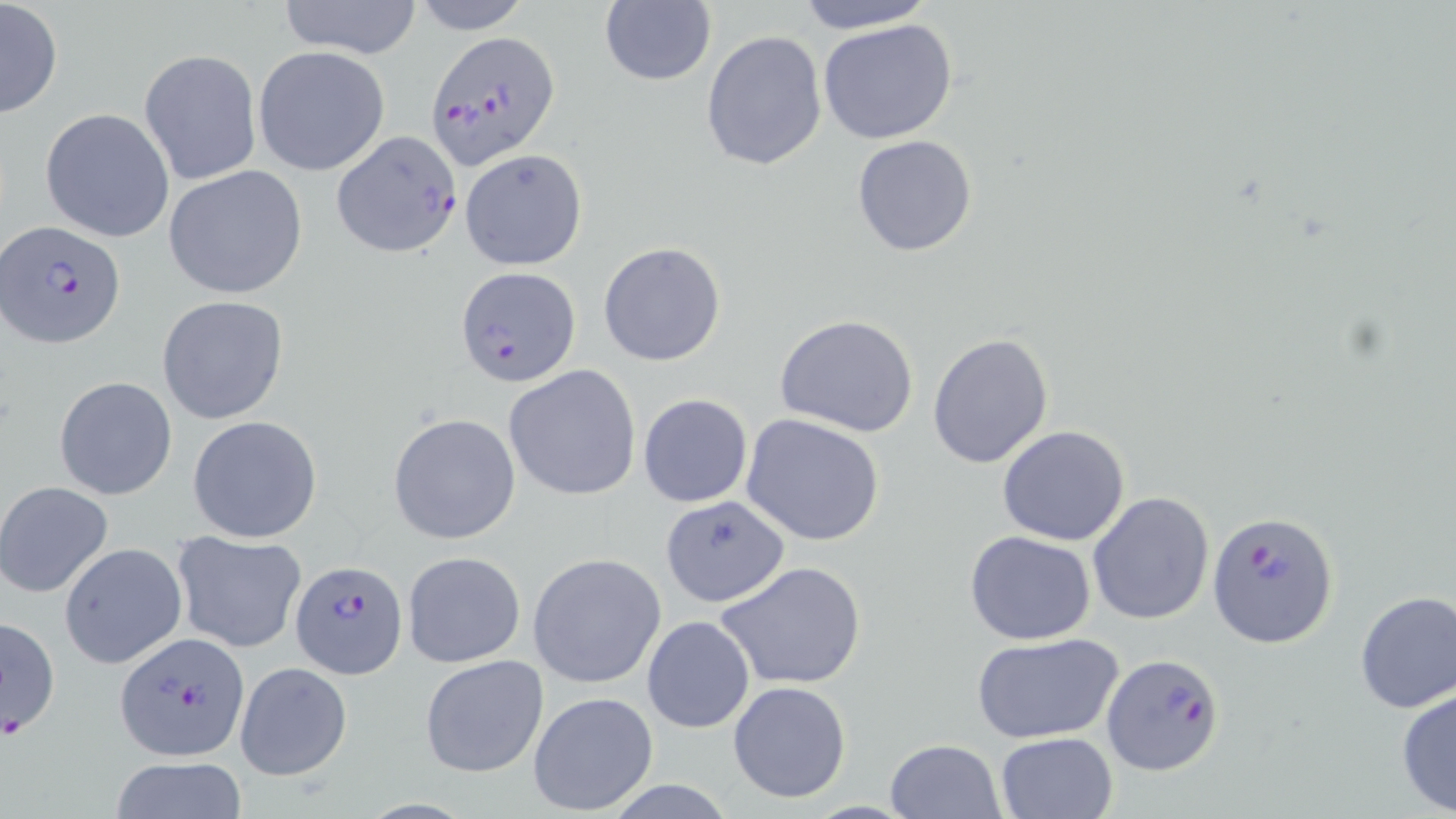

slide-level diagnosis = Plasmodium falciparum
field of view = one of a larger specimen
image size = 1456×819 pixels
preparation = thin blood film
uninfected red blood cell locations = approximate bounding boxes as [x1, y1, x2, y2] in pixels: [1, 0, 63, 121], [277, 0, 423, 59], [599, 0, 717, 87], [795, 0, 934, 33], [409, 1, 534, 33], [816, 17, 959, 146], [700, 29, 828, 173], [252, 45, 392, 178], [139, 48, 261, 186], [40, 108, 175, 242], [851, 134, 978, 257], [459, 149, 587, 270], [163, 165, 309, 300], [598, 241, 727, 367], [156, 295, 291, 426], [774, 313, 921, 439], [928, 332, 1055, 470], [503, 364, 641, 501], [54, 375, 178, 500], [638, 392, 753, 508], [388, 413, 521, 544], [741, 413, 885, 546], [186, 414, 323, 542], [997, 425, 1131, 547], [0, 481, 114, 598], [1087, 492, 1214, 626], [658, 495, 786, 605], [171, 530, 306, 653], [965, 530, 1096, 644], [59, 542, 187, 669], [401, 550, 526, 669], [527, 552, 667, 689], [715, 560, 867, 690], [1353, 591, 1456, 713], [641, 614, 756, 734], [972, 632, 1123, 745], [418, 653, 549, 779], [234, 662, 352, 781], [728, 680, 852, 803], [1395, 686, 1456, 816], [527, 691, 659, 816], [995, 730, 1118, 818], [885, 738, 1006, 819], [107, 757, 249, 819]
stain = May-Grünwald-Giemsa
magnification = 1000x
Plasmodium falciparum-infected red blood cell locations = approximate bounding boxes as [x1, y1, x2, y2] in pixels: [428, 30, 558, 170], [332, 131, 463, 260], [2, 218, 125, 348], [456, 265, 581, 388], [1207, 509, 1338, 651], [291, 559, 408, 680], [1, 615, 61, 739], [113, 632, 251, 762], [1101, 651, 1225, 778]
modality = light microscopy